Report the malaria status of this cell.
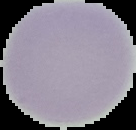

It is uninfected.

Summary:
  - Image type: segmented cell region with the area outside set to black
  - Preparation: thin blood film
  - Image size: 136×130 pixels